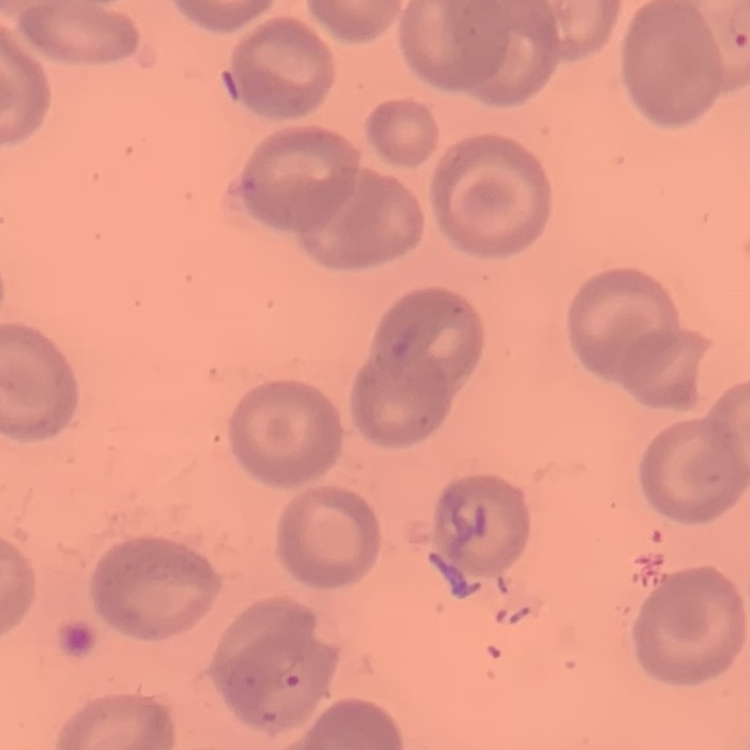
erythrocyte morphology = no rouleaux formation
stain = Field's or Giemsa
image type = square crop of a larger photomicrograph
preparation = thin blood smear